Classify this cell by malaria status.
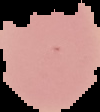

It is uninfected.

{
  "image_type": "cell region segmented out of the field of view; surrounding area masked to black",
  "image_size": "100×112 pixels",
  "preparation": "thin blood film"
}